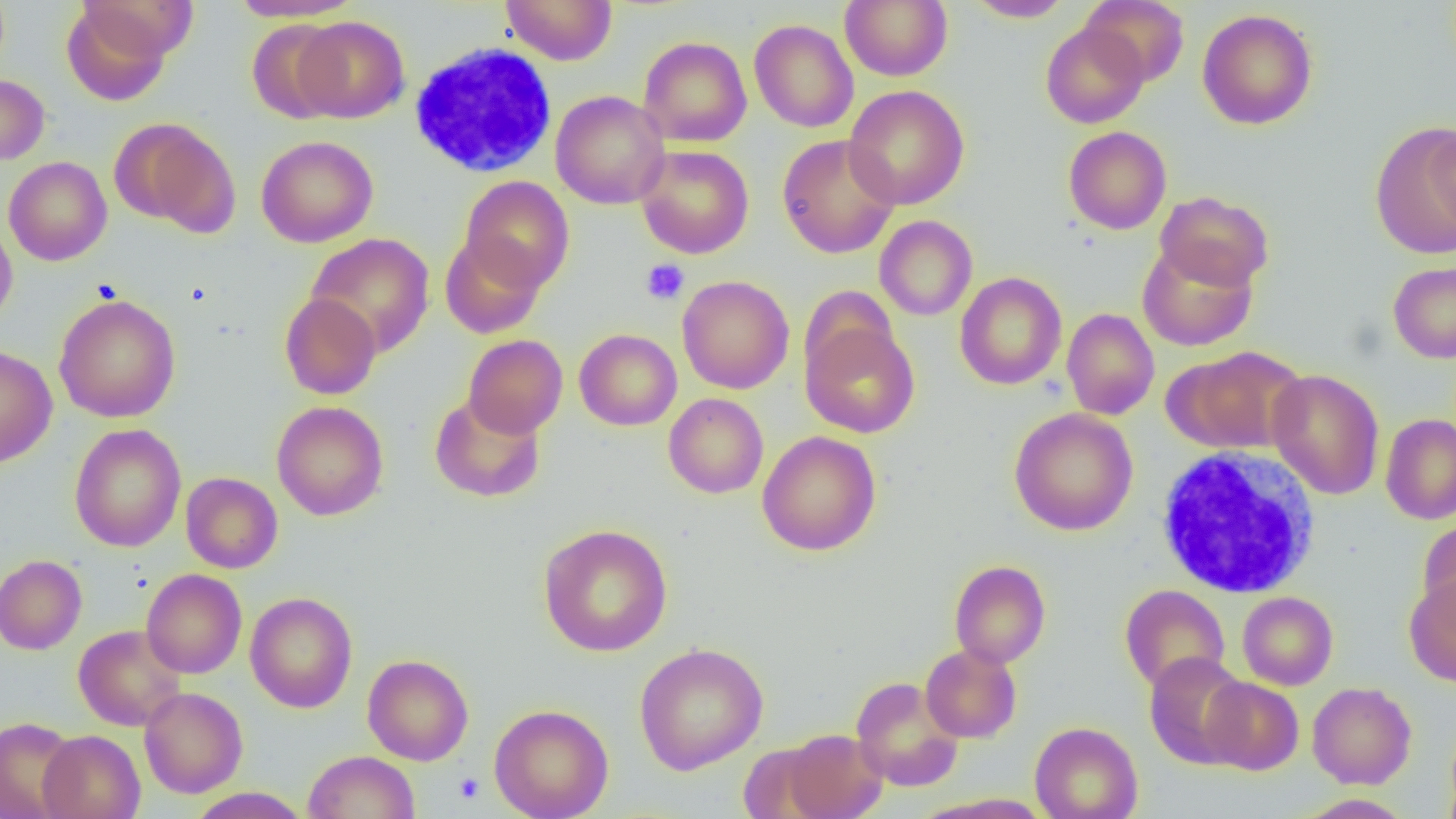

Summary:
  - Coordinate format: approximate bounding boxes as (x1, y1, x2, y2) in pixels
  - Platelet locations: (641, 259, 689, 304), (453, 773, 484, 803)
  - Uninfected red blood cell locations: (229, 0, 364, 22), (501, 0, 618, 65), (964, 0, 1074, 22), (1081, 0, 1189, 86), (840, 1, 952, 81), (61, 2, 178, 106), (1197, 9, 1318, 130), (294, 16, 410, 123), (246, 18, 347, 124), (749, 19, 859, 133), (1040, 22, 1149, 128), (639, 36, 752, 147), (0, 74, 50, 165), (843, 85, 970, 210), (550, 90, 670, 209), (110, 117, 241, 235), (1371, 125, 1456, 258), (1063, 126, 1172, 234), (1425, 126, 1455, 239), (777, 134, 900, 258), (256, 135, 378, 247), (636, 145, 754, 258), (4, 156, 112, 266), (459, 176, 574, 293), (1155, 190, 1274, 292), (875, 215, 977, 321), (0, 216, 17, 330), (439, 232, 546, 339), (305, 233, 435, 357), (1137, 242, 1257, 351), (1388, 261, 1456, 363), (954, 271, 1067, 390), (677, 275, 794, 394), (799, 285, 899, 384), (53, 293, 181, 423), (279, 293, 381, 399), (1062, 308, 1159, 420), (801, 320, 920, 437), (574, 328, 682, 430), (463, 335, 568, 438), (0, 345, 58, 468), (1171, 345, 1307, 453), (1267, 369, 1385, 500), (429, 393, 546, 503), (663, 393, 768, 498), (272, 401, 389, 521), (1009, 408, 1139, 536), (1380, 413, 1456, 525), (69, 423, 186, 552), (757, 430, 881, 556), (180, 472, 283, 573), (1418, 518, 1456, 626), (538, 523, 674, 657), (0, 554, 86, 654), (949, 560, 1051, 668), (141, 568, 247, 679), (1404, 573, 1456, 687), (1119, 584, 1230, 692), (245, 591, 358, 713), (1237, 591, 1338, 690), (73, 624, 186, 731), (633, 643, 769, 774), (920, 644, 1022, 743), (1143, 651, 1250, 769), (362, 654, 474, 765), (851, 676, 964, 791), (1201, 676, 1304, 775), (1307, 682, 1416, 789), (139, 687, 248, 798), (489, 704, 614, 819), (0, 716, 81, 819), (1030, 721, 1143, 819), (1444, 722, 1456, 819), (38, 729, 145, 819), (781, 729, 887, 819), (736, 742, 831, 819), (304, 750, 419, 819), (186, 787, 311, 818), (914, 793, 1055, 819), (1296, 793, 1414, 818)
  - White blood cell locations: (408, 42, 558, 179), (1156, 446, 1321, 598)
  - Slide-level diagnosis: negative for blood parasites
  - Field of view: one of a larger specimen
  - Image size: 1456×819 pixels
  - Magnification: 1000x
  - Modality: light microscopy
  - Preparation: thin blood smear